Assess for parasitized red blood cells.
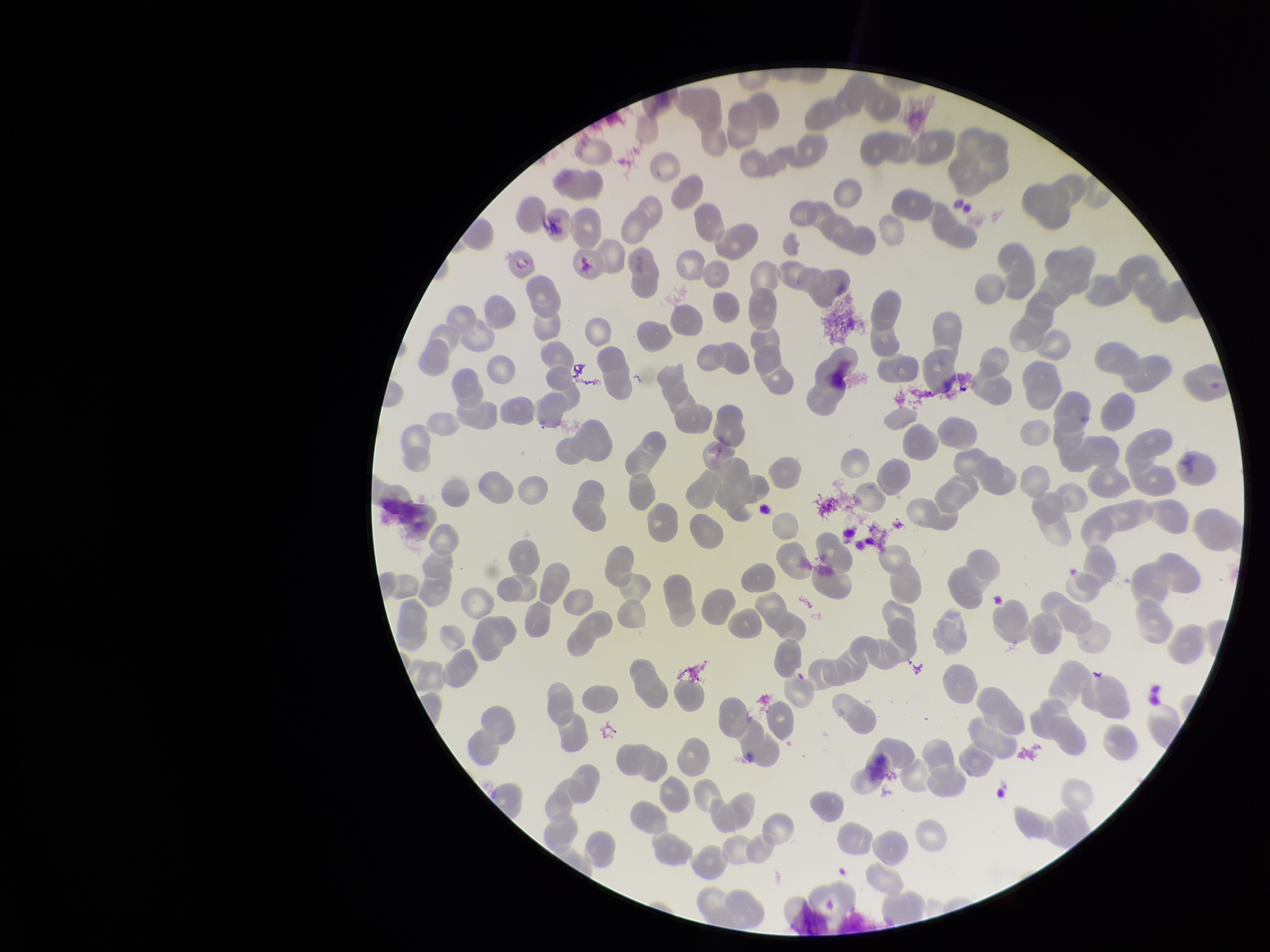

None identified.

patient_malaria_status: negative
red_blood_cell_count: 252
parasitized_red_blood_cell_count: 0
stain: Giemsa
capture: smartphone photograph through the microscope eyepiece
field_of_view: one from this slide
image_size: 1270×952 pixels
preparation: thin